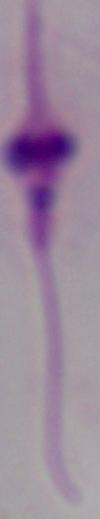

Photomicrograph. A Leishmania parasite is seen. 1000x magnification.